Report the malaria status of this cell.
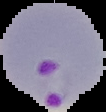
It is parasitized.

image_type: segmented cell region with the area outside set to black
preparation: thin blood smear
image_size: 106×112 pixels